State the blood parasite species.
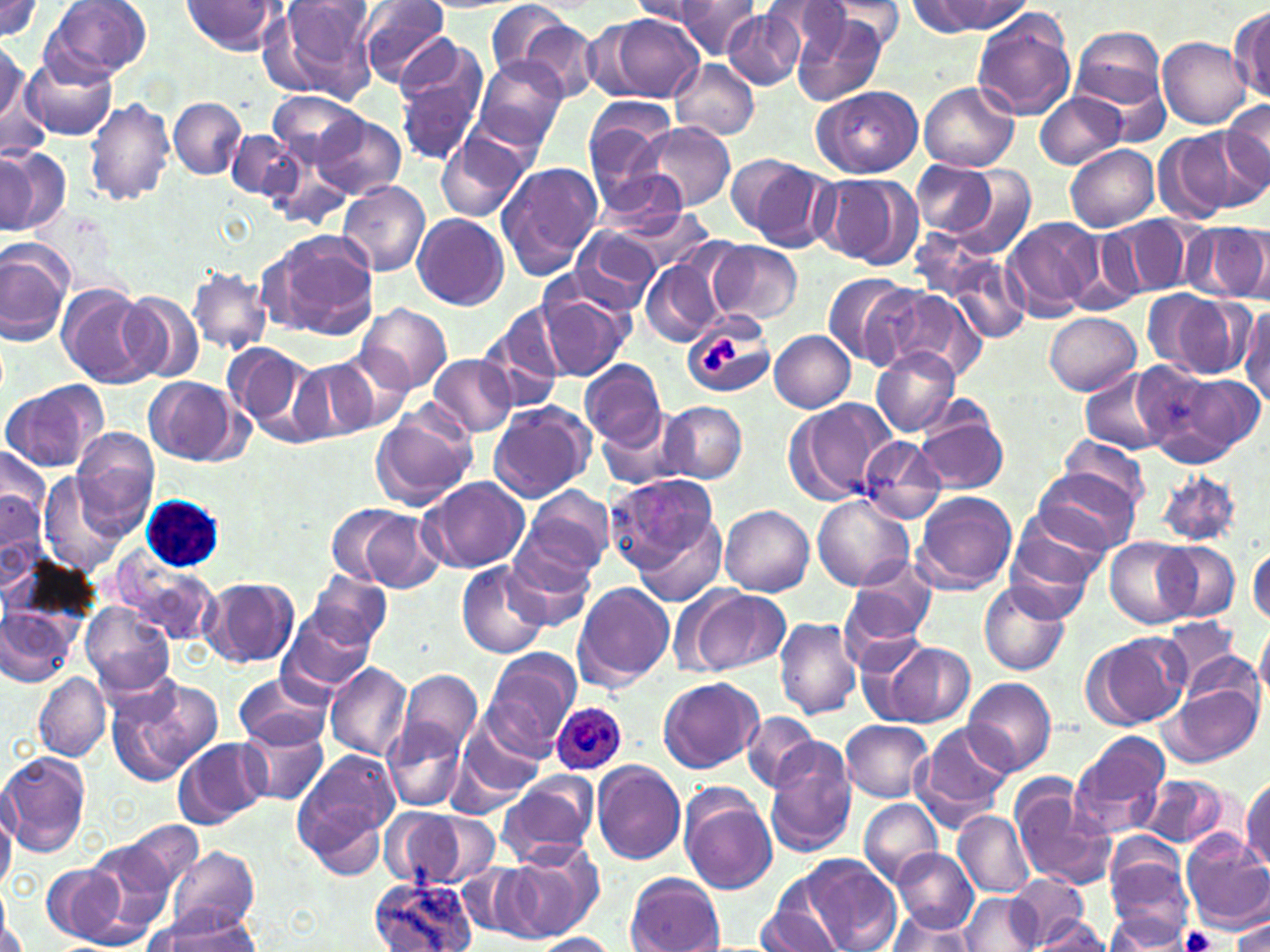

Plasmodium ovale.

Summary:
  - Coordinate format: approximate bounding boxes as (x1,y1)-(x2,y2) corner pairs in pixels
  - Platelet locations: (698,335)-(738,374), (1180,928)-(1220,952)
  - Plasmodium ovale-infected red blood cell locations: (550,702)-(626,777)
  - Uninfected red blood cell locations: (0,0)-(45,44), (271,0)-(378,101), (357,0)-(452,86), (41,1)-(153,85), (179,1)-(283,55), (631,1)-(714,25), (674,1)-(762,60), (762,1)-(852,58), (925,1)-(1030,34), (488,2)-(579,82), (820,3)-(908,52), (724,7)-(806,89), (1231,7)-(1270,102), (791,8)-(888,106), (971,10)-(1075,120), (590,13)-(704,105), (521,20)-(601,101), (1070,26)-(1168,120), (396,33)-(479,116), (1158,35)-(1253,130), (0,41)-(35,150), (395,53)-(485,166), (24,56)-(118,140), (470,57)-(570,152), (670,59)-(760,140), (920,83)-(1019,172), (811,85)-(923,179), (1035,91)-(1124,168), (268,92)-(365,167), (85,97)-(177,207), (584,97)-(677,177), (168,98)-(247,178), (1219,99)-(1270,200), (313,114)-(405,199), (634,122)-(736,211), (226,127)-(305,203), (1152,129)-(1248,223), (436,135)-(530,223), (1065,144)-(1160,231), (266,145)-(353,228), (0,150)-(49,234), (728,154)-(836,249), (908,157)-(1032,256), (496,162)-(604,277), (590,166)-(692,237), (814,173)-(921,270), (337,181)-(431,277), (601,204)-(717,279), (411,213)-(509,310), (1106,216)-(1196,297), (1002,218)-(1103,321), (1185,220)-(1270,303), (567,227)-(664,313), (264,229)-(381,339), (709,241)-(802,324), (0,244)-(73,345), (921,248)-(1032,345), (640,258)-(724,347), (188,265)-(271,355), (822,272)-(915,368), (867,285)-(987,382), (533,287)-(635,381), (61,289)-(157,387), (116,289)-(205,387), (1148,293)-(1247,379), (1236,303)-(1270,408), (358,304)-(451,393), (478,306)-(570,411), (1043,310)-(1140,395), (682,314)-(775,402), (769,330)-(856,413), (222,342)-(323,440), (334,347)-(415,433), (872,347)-(960,437), (428,354)-(517,437), (289,357)-(375,443), (581,359)-(666,446), (1134,363)-(1259,468), (1080,368)-(1173,456), (143,377)-(243,464), (2,379)-(109,474), (783,399)-(894,505), (487,402)-(596,504), (661,402)-(747,484), (595,407)-(701,492), (913,408)-(1010,495), (371,411)-(476,511), (72,431)-(160,531), (857,437)-(947,525), (1056,437)-(1152,520), (1,445)-(51,556), (1031,465)-(1142,556), (1154,470)-(1243,548), (41,472)-(128,577), (603,472)-(724,587), (421,476)-(530,573), (521,484)-(616,579), (912,492)-(1018,595), (811,494)-(916,593), (1,496)-(48,589), (333,503)-(445,594), (720,505)-(814,595), (1005,507)-(1109,611), (1106,537)-(1197,628), (500,539)-(598,632), (1161,544)-(1239,621), (1247,546)-(1270,626), (113,555)-(219,648), (456,561)-(551,660), (839,561)-(938,660), (304,570)-(391,651), (200,577)-(300,669), (571,582)-(675,690), (979,584)-(1072,675), (681,587)-(791,676), (81,602)-(177,697), (0,604)-(75,690), (279,604)-(379,698), (774,617)-(862,719), (1159,619)-(1245,695), (1255,627)-(1270,708), (1083,632)-(1191,730), (876,641)-(975,728), (485,649)-(579,752), (324,662)-(412,761), (397,670)-(483,757), (34,672)-(110,762), (107,673)-(225,784), (234,673)-(334,750), (962,676)-(1057,776), (658,677)-(763,773), (1157,677)-(1264,769), (742,712)-(822,792), (841,719)-(933,802), (383,720)-(467,812), (913,722)-(1014,825), (235,724)-(330,806), (456,724)-(545,802), (1072,731)-(1172,837), (176,737)-(266,827), (764,743)-(857,858), (0,751)-(91,858), (293,752)-(400,866), (591,760)-(688,867), (498,772)-(598,867), (1139,773)-(1231,851), (1243,776)-(1270,875), (1010,780)-(1118,890), (679,789)-(777,894), (0,797)-(16,895), (859,798)-(942,885), (384,809)-(464,887), (953,811)-(1035,897), (412,812)-(501,888), (120,820)-(203,894), (1180,830)-(1270,929), (1103,834)-(1194,937), (86,839)-(178,932), (506,841)-(603,938), (171,845)-(259,934), (891,847)-(979,934), (801,853)-(904,952), (41,862)-(132,947), (625,872)-(725,952), (1004,874)-(1090,949), (369,876)-(475,952), (960,893)-(1038,951), (0,897)-(22,952), (756,899)-(848,952), (142,908)-(266,950), (885,909)-(980,952), (1104,909)-(1196,950), (1232,916)-(1270,952), (1034,917)-(1111,950), (531,932)-(617,951)
  - Modality: light microscopy
  - Preparation: thin blood smear
  - Image size: 1270×952 pixels
  - Magnification: 1000x
  - Field of view: single
  - Stain: May-Grünwald-Giemsa